Outline each blood parasite and name the species.
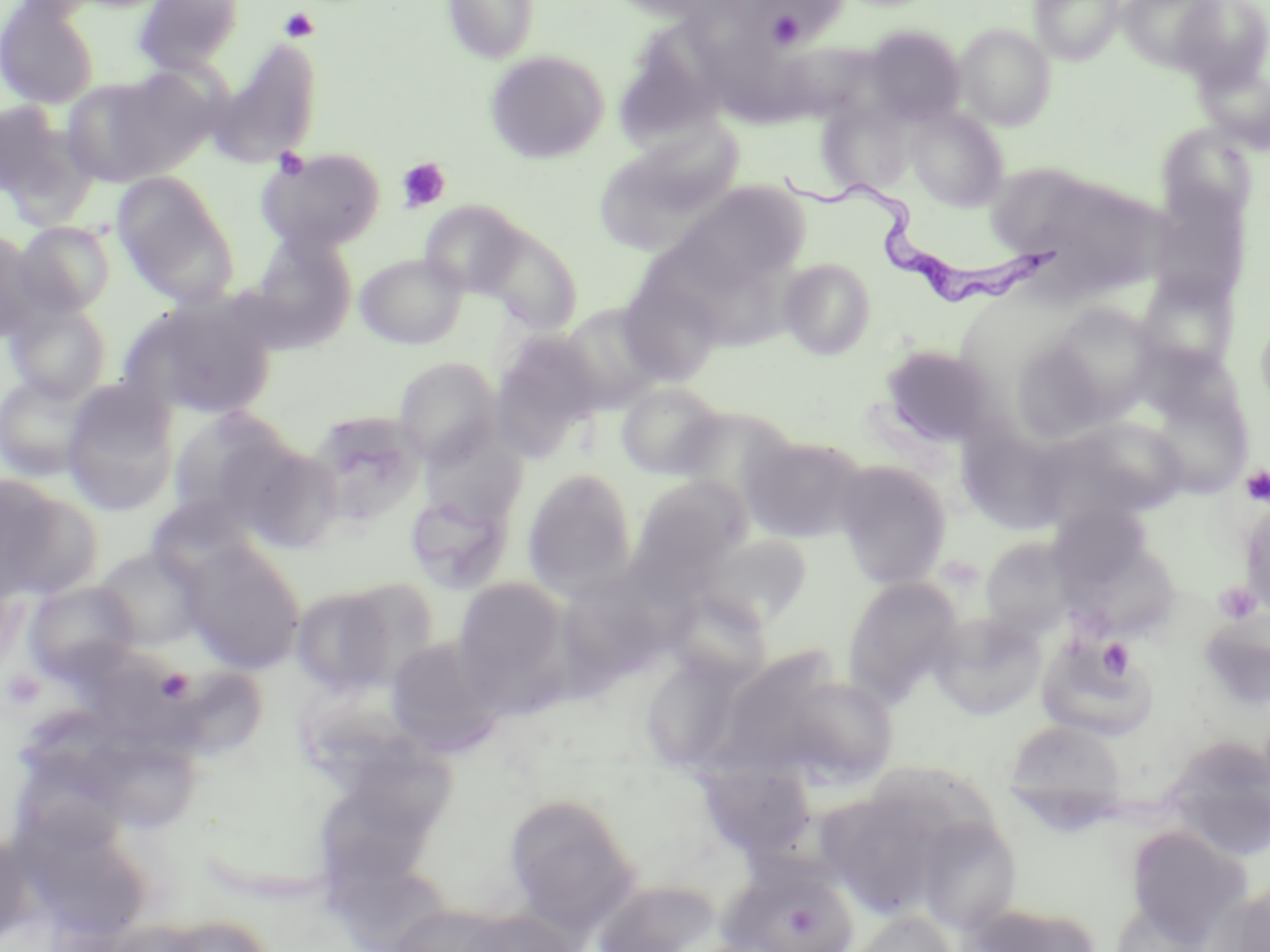
Approximate bounding boxes as [x1, y1, x2, y2] in pixels.
Trypanosoma brucei: [789, 172, 1061, 309].
No Plasmodium falciparum, Plasmodium ovale, Plasmodium malariae, Plasmodium vivax, or Babesia divergens observed.

Uninfected red blood cell locations: [133, 0, 246, 75], [603, 0, 741, 23], [1029, 0, 1125, 65], [1117, 0, 1225, 72], [1170, 0, 1270, 89], [0, 1, 101, 108], [444, 1, 540, 64], [745, 1, 842, 49], [954, 24, 1055, 130], [863, 25, 966, 126], [613, 27, 731, 151], [210, 40, 323, 167], [485, 50, 609, 164], [1197, 61, 1270, 153], [61, 75, 184, 188], [0, 97, 88, 215], [816, 100, 913, 197], [905, 107, 1010, 211], [1157, 125, 1257, 226], [641, 127, 747, 212], [257, 147, 386, 253], [592, 158, 713, 255], [986, 163, 1106, 261], [112, 172, 237, 304], [671, 182, 807, 289], [1146, 185, 1251, 311], [419, 199, 527, 298], [14, 222, 116, 318], [476, 223, 583, 334], [0, 230, 49, 343], [245, 234, 357, 352], [356, 253, 466, 349], [778, 258, 877, 360], [616, 273, 726, 387], [1133, 274, 1239, 378], [126, 297, 280, 420], [4, 300, 112, 404], [557, 304, 667, 413], [1041, 304, 1162, 423], [1254, 306, 1270, 419], [489, 329, 607, 456], [1006, 335, 1119, 445], [1134, 343, 1245, 431], [879, 344, 1001, 449], [394, 357, 502, 466], [0, 373, 98, 481], [61, 380, 180, 516], [615, 382, 727, 480], [1145, 389, 1252, 499], [669, 407, 799, 513], [166, 408, 297, 522], [306, 411, 426, 529], [1065, 417, 1188, 519], [958, 428, 1071, 534], [419, 432, 528, 527], [742, 434, 867, 543], [230, 440, 345, 553], [832, 461, 952, 589], [522, 468, 637, 594], [0, 475, 87, 599], [630, 477, 749, 582], [404, 491, 513, 594], [145, 493, 262, 588], [1239, 499, 1270, 622], [697, 533, 814, 628], [981, 537, 1075, 638], [179, 541, 307, 674], [93, 547, 206, 650], [53, 569, 189, 673], [556, 571, 683, 686], [452, 576, 572, 705], [842, 577, 964, 704], [23, 581, 140, 682], [292, 586, 402, 696], [664, 590, 773, 688], [1197, 611, 1270, 714], [927, 612, 1048, 721], [1037, 633, 1159, 741], [385, 637, 507, 757], [639, 655, 746, 774], [160, 665, 263, 759], [796, 686, 898, 783], [1003, 719, 1128, 820], [93, 734, 200, 840], [1161, 735, 1270, 862], [355, 740, 464, 838], [19, 758, 128, 861], [699, 763, 817, 858], [318, 789, 429, 883], [816, 791, 948, 919], [503, 792, 641, 934], [916, 817, 1022, 934], [1125, 827, 1250, 943], [33, 831, 142, 940], [722, 863, 859, 952], [591, 879, 721, 952], [1213, 884, 1270, 950], [964, 903, 1101, 952], [442, 908, 588, 952], [847, 911, 957, 952], [155, 915, 280, 952]. Platelet locations: [754, 4, 818, 50], [279, 7, 319, 42], [273, 148, 310, 180], [396, 158, 451, 212], [1240, 465, 1270, 506], [1213, 582, 1261, 626], [1098, 637, 1134, 679], [155, 667, 194, 704], [3, 669, 45, 713]. Slide-level diagnosis: Trypanosoma brucei. May-Grünwald-Giemsa stain. Thin blood film. Image is 1270×952 pixels. Light microscopy. One field of a larger specimen. Captured at 1000x magnification.